Give the extent of all Plasmodium ovale-infected red blood cells.
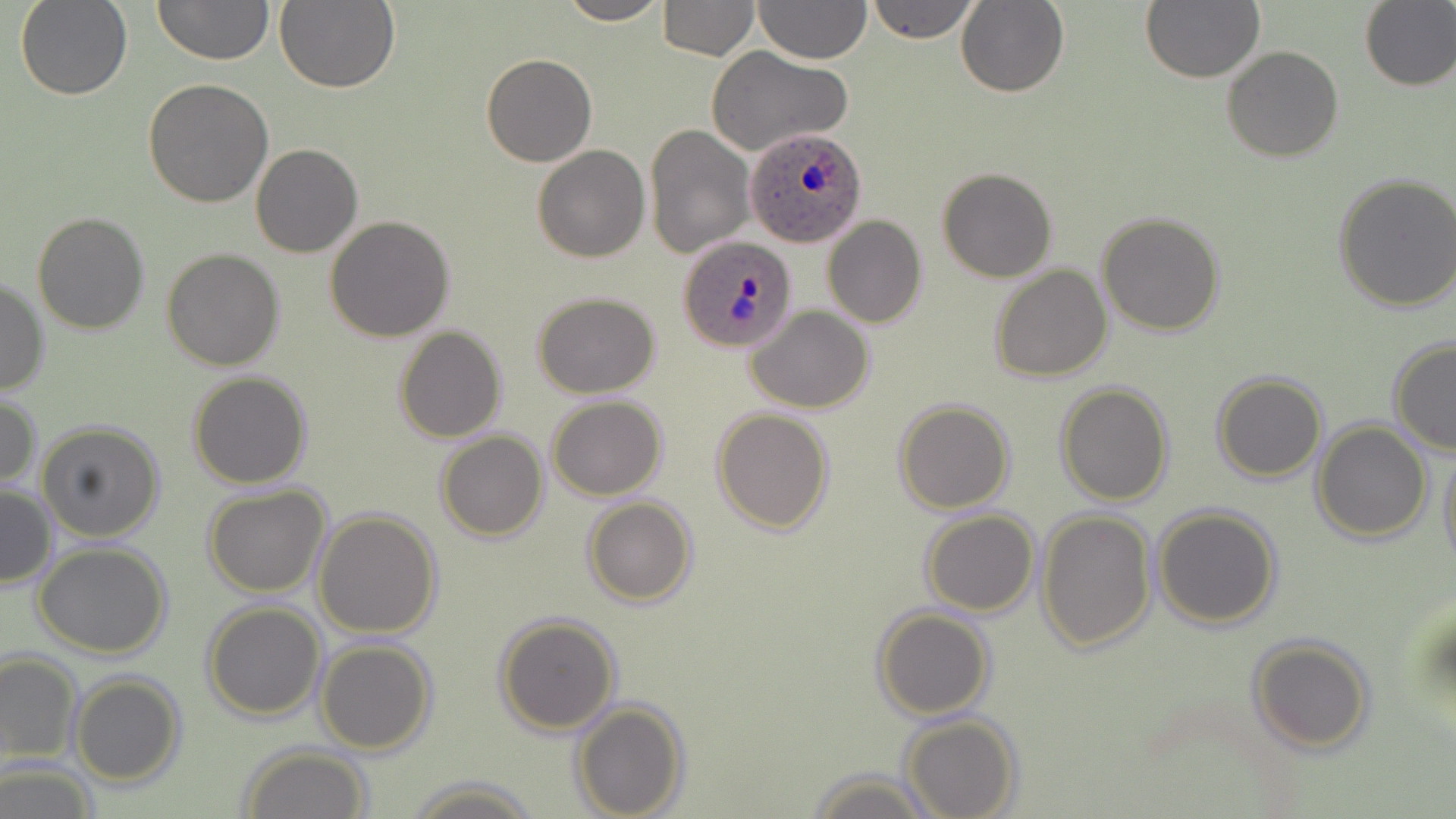
Approximate bounding boxes as named x1/y1/x2/y2 corners in pixels.
Plasmodium ovale-infected red blood cells: (x1=746, y1=125, x2=868, y2=248), (x1=678, y1=234, x2=798, y2=353).

slide-level diagnosis = Plasmodium ovale
modality = optical microscopy
preparation = thin blood film
field of view = single
image size = 1456×819 pixels
stain = May-Grünwald-Giemsa
uninfected red blood cell locations = approximate bounding boxes as named x1/y1/x2/y2 corners in pixels: (x1=15, y1=0, x2=132, y2=100), (x1=153, y1=0, x2=273, y2=66), (x1=275, y1=0, x2=401, y2=95), (x1=555, y1=0, x2=670, y2=26), (x1=657, y1=0, x2=759, y2=59), (x1=753, y1=0, x2=871, y2=65), (x1=866, y1=0, x2=980, y2=44), (x1=1141, y1=0, x2=1264, y2=83), (x1=957, y1=1, x2=1070, y2=97), (x1=1358, y1=1, x2=1456, y2=91), (x1=1222, y1=46, x2=1344, y2=162), (x1=706, y1=47, x2=851, y2=158), (x1=481, y1=53, x2=597, y2=167), (x1=143, y1=79, x2=274, y2=207), (x1=645, y1=122, x2=756, y2=259), (x1=250, y1=144, x2=363, y2=258), (x1=532, y1=145, x2=650, y2=262), (x1=936, y1=167, x2=1058, y2=282), (x1=1334, y1=172, x2=1456, y2=312), (x1=32, y1=210, x2=152, y2=334), (x1=1096, y1=212, x2=1225, y2=335), (x1=325, y1=215, x2=455, y2=341), (x1=824, y1=216, x2=927, y2=329), (x1=162, y1=247, x2=285, y2=370), (x1=170, y1=250, x2=295, y2=489), (x1=990, y1=265, x2=1112, y2=382), (x1=0, y1=275, x2=49, y2=397), (x1=533, y1=292, x2=660, y2=398), (x1=747, y1=306, x2=876, y2=414), (x1=392, y1=325, x2=508, y2=442), (x1=1388, y1=338, x2=1456, y2=455), (x1=187, y1=371, x2=313, y2=489), (x1=1212, y1=371, x2=1327, y2=482), (x1=1054, y1=382, x2=1174, y2=505), (x1=0, y1=393, x2=41, y2=492), (x1=548, y1=396, x2=667, y2=500), (x1=894, y1=398, x2=1015, y2=513), (x1=711, y1=408, x2=834, y2=533), (x1=1311, y1=419, x2=1433, y2=543), (x1=36, y1=421, x2=165, y2=542), (x1=435, y1=429, x2=549, y2=541), (x1=1438, y1=439, x2=1456, y2=570), (x1=1, y1=483, x2=57, y2=590), (x1=203, y1=485, x2=331, y2=598), (x1=582, y1=497, x2=698, y2=606), (x1=1152, y1=504, x2=1282, y2=629), (x1=313, y1=509, x2=443, y2=638), (x1=1037, y1=509, x2=1156, y2=653), (x1=920, y1=510, x2=1038, y2=616), (x1=33, y1=543, x2=172, y2=659), (x1=202, y1=600, x2=326, y2=720), (x1=872, y1=606, x2=993, y2=720), (x1=493, y1=612, x2=621, y2=735), (x1=1247, y1=636, x2=1375, y2=754), (x1=314, y1=639, x2=436, y2=754), (x1=0, y1=651, x2=82, y2=767), (x1=70, y1=674, x2=186, y2=786), (x1=571, y1=698, x2=688, y2=818), (x1=900, y1=714, x2=1021, y2=819), (x1=239, y1=745, x2=372, y2=819), (x1=0, y1=762, x2=99, y2=819), (x1=808, y1=768, x2=935, y2=819), (x1=403, y1=774, x2=543, y2=817)
magnification = 1000x